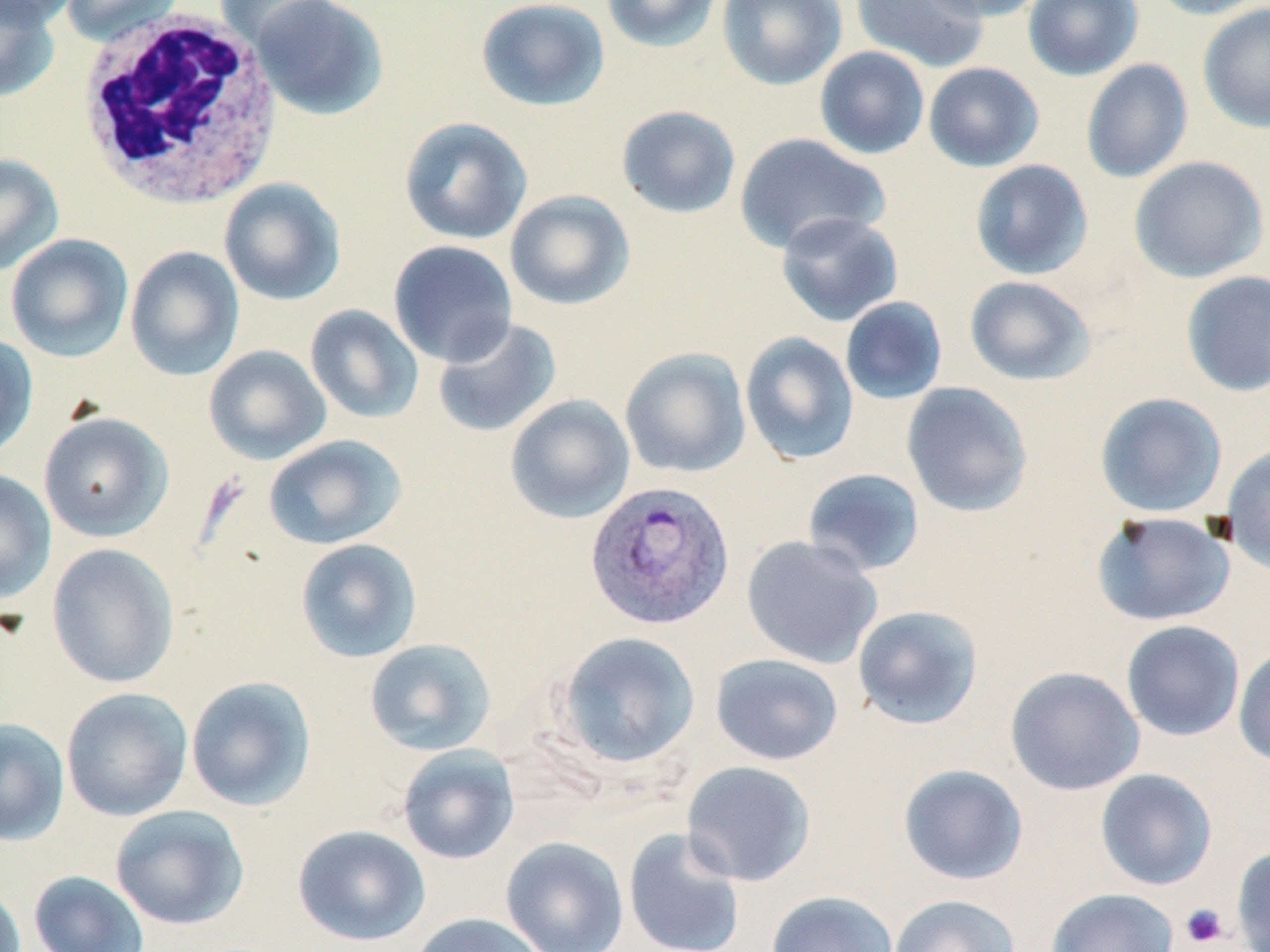
Summary:
  - Coordinate format: approximate bounding boxes as (x1, y1, x2, y2) in pixels
  - Uninfected red blood cell locations: (0, 0, 80, 28), (0, 0, 60, 103), (60, 0, 185, 46), (214, 0, 339, 53), (249, 0, 389, 120), (475, 0, 611, 111), (601, 0, 723, 53), (717, 0, 846, 91), (852, 0, 990, 72), (918, 0, 1048, 21), (1023, 0, 1143, 81), (1145, 0, 1269, 20), (1198, 2, 1270, 133), (815, 46, 930, 159), (1081, 59, 1193, 183), (923, 62, 1044, 172), (616, 105, 741, 219), (399, 116, 533, 245), (733, 133, 891, 255), (0, 153, 64, 277), (1128, 156, 1268, 283), (970, 160, 1093, 280), (219, 178, 346, 305), (504, 190, 636, 310), (775, 211, 903, 326), (5, 233, 134, 362), (387, 240, 518, 367), (125, 246, 245, 381), (1181, 270, 1270, 396), (964, 275, 1096, 386), (839, 296, 948, 405), (305, 304, 424, 424), (431, 317, 562, 438), (740, 331, 859, 465), (0, 333, 39, 462), (204, 345, 332, 465), (620, 347, 751, 478), (901, 382, 1034, 518), (1095, 392, 1228, 518), (505, 395, 635, 523), (38, 411, 173, 542), (263, 434, 407, 550), (1221, 445, 1270, 577), (802, 468, 926, 577), (0, 470, 57, 603), (1092, 511, 1235, 626), (741, 535, 883, 668), (295, 538, 422, 663), (47, 543, 180, 688), (852, 605, 984, 730), (1121, 620, 1245, 742), (554, 631, 701, 770), (364, 638, 497, 756), (1233, 646, 1270, 767), (711, 653, 844, 766), (1005, 666, 1145, 796), (185, 676, 317, 811), (61, 687, 193, 821), (0, 718, 70, 846), (397, 744, 520, 865), (681, 760, 816, 886), (898, 764, 1028, 885), (1095, 768, 1217, 891), (110, 804, 250, 930), (292, 824, 431, 946), (623, 827, 746, 952), (500, 836, 629, 952), (1232, 844, 1270, 952), (28, 870, 150, 952), (0, 880, 26, 952), (1046, 888, 1179, 951), (766, 890, 898, 952), (888, 894, 1021, 952), (408, 912, 549, 952)
  - Platelet locations: (1180, 903, 1229, 948)
  - Plasmodium vivax-infected red blood cell locations: (587, 487, 736, 638)
  - White blood cell locations: (75, 11, 284, 211)
  - Slide-level diagnosis: Plasmodium vivax
  - Preparation: thin blood film
  - Magnification: 1000x
  - Stain: May-Grünwald-Giemsa
  - Field of view: single
  - Modality: optical microscopy
  - Image size: 1270×952 pixels